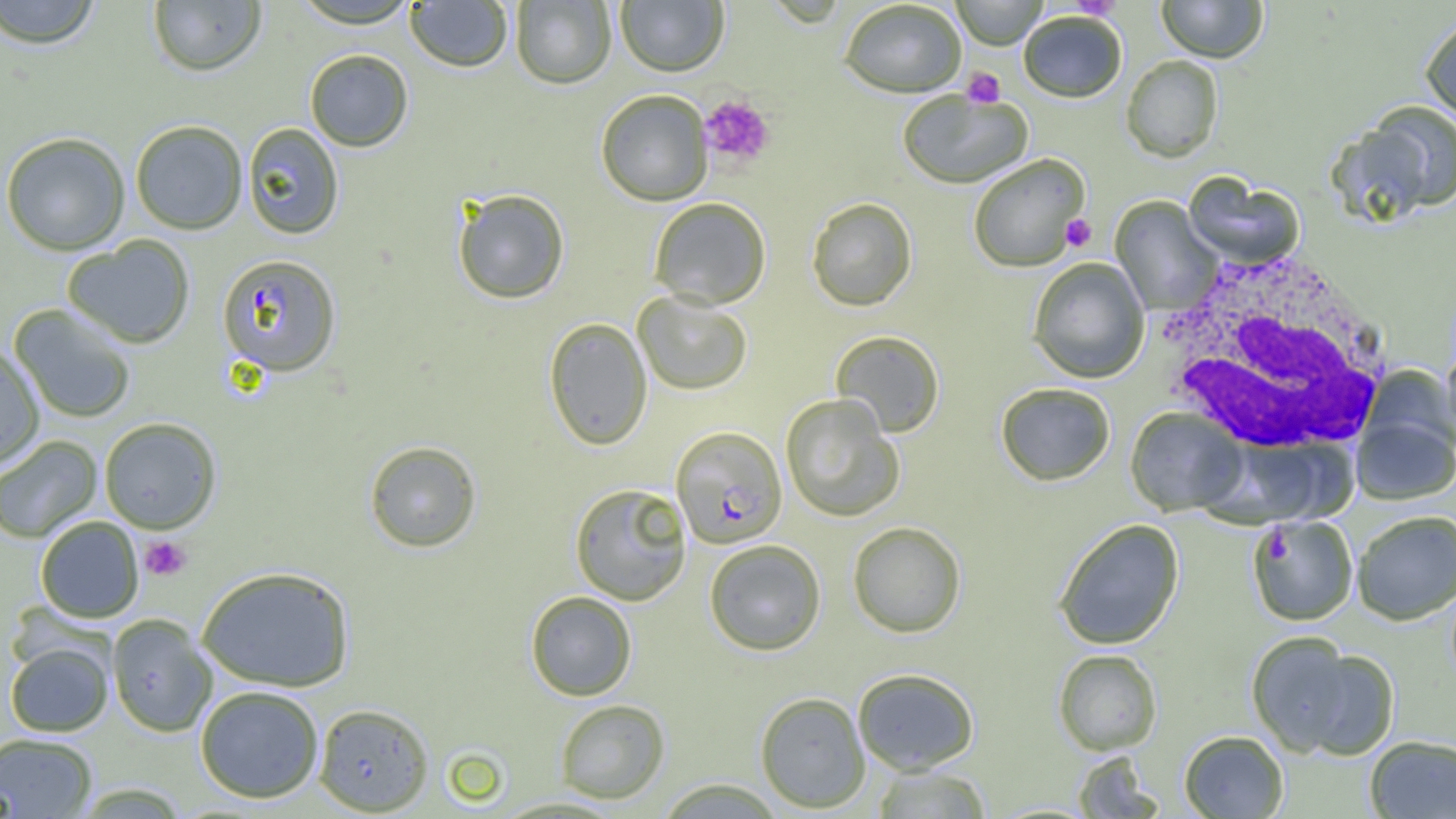

Summary:
  - Coordinate format: approximate bounding boxes as (x1, y1, x2, y2) in pixels
  - White blood cell locations: (1154, 249, 1395, 456)
  - Platelet locations: (1069, 0, 1122, 20), (962, 67, 1005, 108), (699, 95, 775, 169), (1060, 214, 1096, 252), (140, 536, 192, 581)
  - Uninfected red blood cell locations: (0, 0, 104, 49), (291, 0, 421, 30), (511, 0, 617, 89), (615, 0, 729, 77), (950, 0, 1049, 50), (1156, 0, 1268, 63), (148, 1, 266, 76), (405, 1, 513, 72), (839, 2, 967, 99), (1018, 11, 1127, 104), (1420, 14, 1456, 124), (304, 49, 414, 152), (1121, 56, 1223, 163), (595, 90, 713, 206), (897, 90, 1033, 189), (1361, 103, 1456, 214), (130, 120, 248, 234), (242, 123, 345, 240), (0, 132, 131, 255), (968, 154, 1090, 273), (1183, 174, 1304, 270), (452, 188, 570, 305), (1110, 196, 1223, 316), (649, 197, 771, 309), (806, 198, 917, 312), (61, 236, 195, 348), (1027, 257, 1150, 384), (633, 292, 753, 396), (8, 304, 137, 424), (543, 317, 652, 451), (830, 330, 945, 438), (0, 343, 45, 468), (1441, 348, 1456, 448), (1359, 366, 1455, 466), (995, 383, 1115, 486), (780, 394, 905, 522), (1125, 408, 1248, 516), (1352, 414, 1455, 505), (99, 417, 222, 533), (0, 435, 102, 544), (364, 441, 482, 552), (569, 483, 692, 605), (1352, 510, 1456, 625), (1249, 515, 1358, 626), (35, 516, 144, 623), (1053, 518, 1185, 650), (848, 521, 966, 637), (704, 539, 826, 656), (196, 565, 356, 691), (525, 591, 637, 701), (107, 614, 217, 737), (1246, 631, 1363, 756), (5, 641, 114, 736), (1291, 644, 1400, 761), (1053, 649, 1162, 755), (852, 667, 980, 774), (195, 685, 324, 803), (754, 691, 871, 812), (555, 699, 670, 803), (313, 702, 435, 815), (1179, 730, 1288, 818), (0, 732, 97, 818), (1364, 735, 1456, 818), (1072, 751, 1164, 818), (871, 765, 992, 818), (653, 778, 787, 818)
  - Plasmodium falciparum-infected red blood cell locations: (216, 253, 342, 376), (670, 426, 788, 549)
  - Slide-level diagnosis: Plasmodium falciparum
  - Image size: 1456×819 pixels
  - Preparation: thin blood smear
  - Field of view: one of a larger specimen
  - Modality: optical microscopy
  - Magnification: 1000x